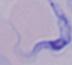
modality = photomicrograph
identification = trypanosome
magnification = 1000x